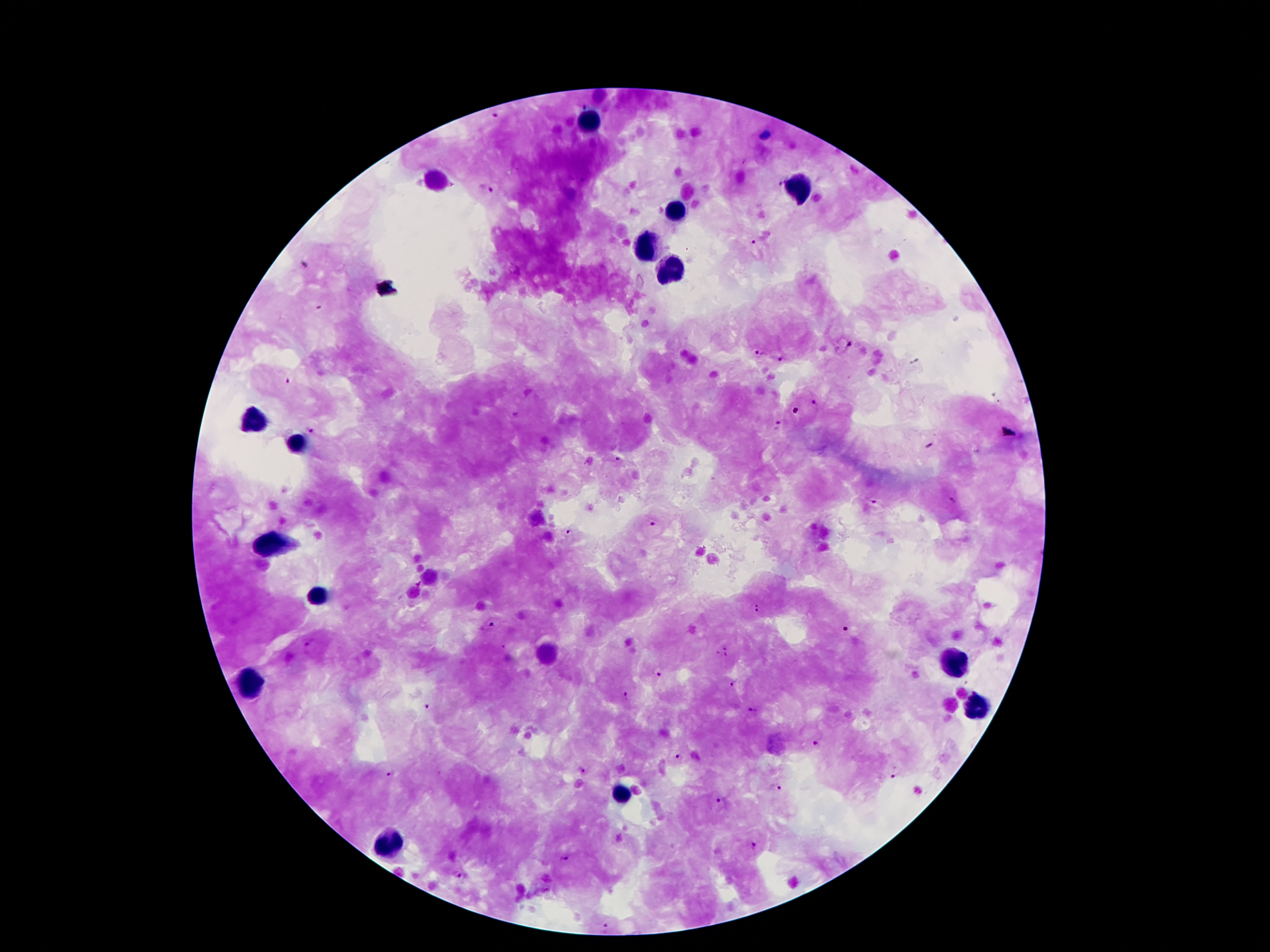 Approximate object centers, in pixels from the top-left corner. Plasmodium parasite locations: (x=780, y=182), (x=486, y=187), (x=751, y=243), (x=848, y=344), (x=758, y=353), (x=781, y=361), (x=288, y=381), (x=815, y=403), (x=516, y=415), (x=777, y=425), (x=310, y=431), (x=618, y=458), (x=952, y=500), (x=872, y=501), (x=652, y=525), (x=567, y=532), (x=755, y=610), (x=491, y=626), (x=846, y=629), (x=309, y=641), (x=659, y=676), (x=734, y=684), (x=623, y=696), (x=426, y=703), (x=754, y=711), (x=817, y=743), (x=676, y=756), (x=392, y=771), (x=582, y=771), (x=893, y=776), (x=778, y=788), (x=718, y=802), (x=756, y=847), (x=564, y=859), (x=464, y=876), (x=605, y=927). Leukocyte locations: (x=585, y=116), (x=435, y=178), (x=800, y=192), (x=674, y=211), (x=645, y=245), (x=663, y=273), (x=256, y=424), (x=298, y=444), (x=276, y=543), (x=315, y=600), (x=952, y=660), (x=249, y=684), (x=977, y=709), (x=623, y=793), (x=393, y=842). Smartphone photograph taken through the microscope eyepiece. Giemsa-stained preparation. Thick blood film. Patient malaria status: infected with Plasmodium falciparum. 100x magnification. Single field of view. Image is 1270×952 pixels.